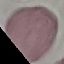
Summary:
  - Result: no malaria parasites seen
  - Capture: smartphone through the microscope eyepiece
  - Preparation: thin blood smear
  - Stain: Giemsa
  - Image type: cell patch, automatically extracted from a larger field of view and resized to 64 × 64 pixels